Draw a bounding box around every leukocyte (white blood cell).
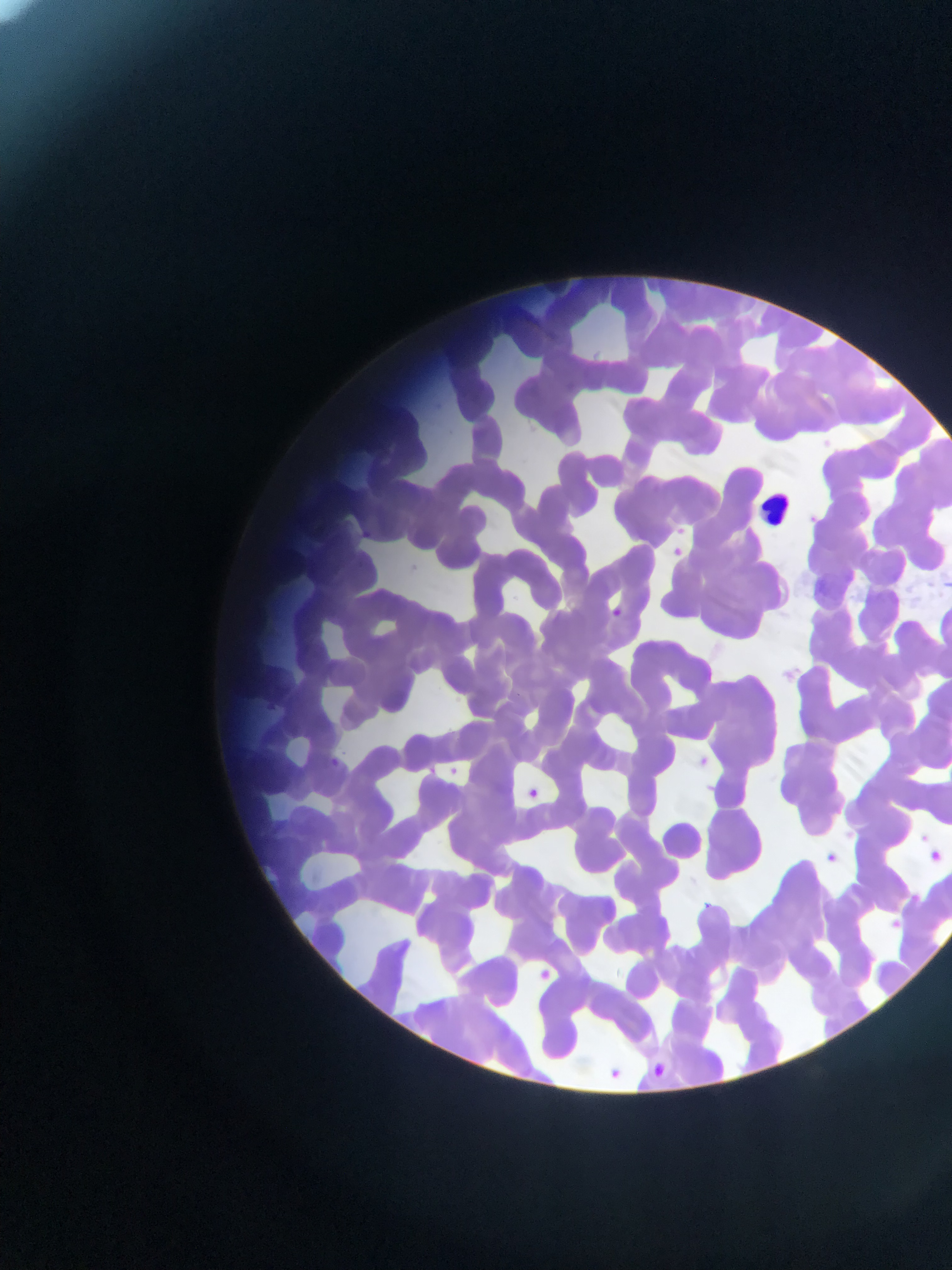

Approximate bounding boxes as (left, top, right, bottom) in pixels.
Leukocytes: (758, 490, 798, 531).

Summary:
  - Plasmodium parasite locations: (674, 516, 689, 537), (673, 546, 686, 558), (610, 609, 629, 617), (692, 751, 711, 768), (330, 756, 350, 779), (446, 759, 463, 780), (422, 765, 436, 780), (531, 782, 545, 801), (922, 830, 930, 840), (931, 846, 945, 862), (829, 851, 843, 866), (705, 898, 723, 917), (884, 904, 901, 929), (535, 960, 562, 989), (653, 1058, 679, 1084), (613, 1064, 625, 1075)
  - Country: Ghana
  - Field of view: single
  - Capture: mobile-phone photograph through a microscope
  - Image size: 952×1270 pixels
  - Preparation: thin blood smear